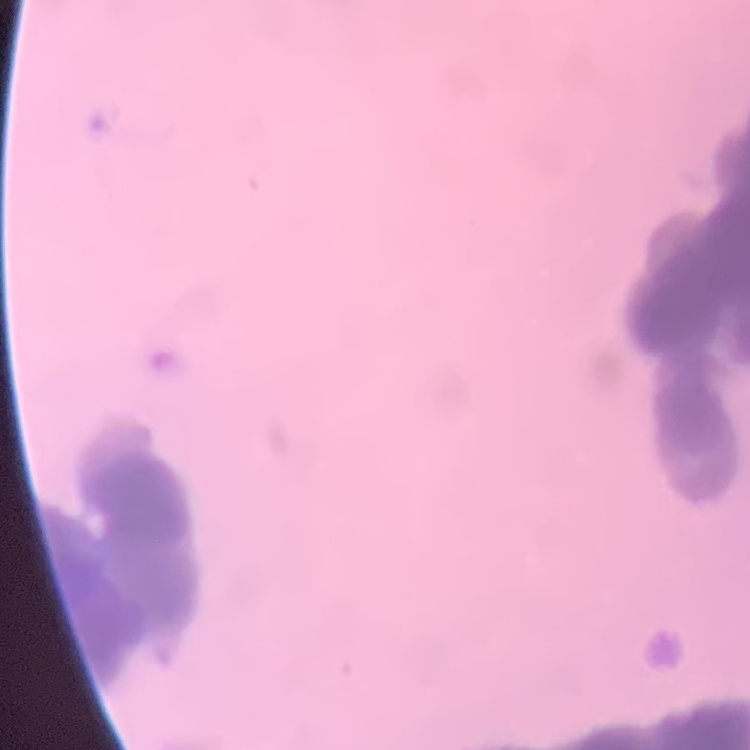

The red blood cells show rouleaux formation. Thin peripheral smear. One tile cut from a larger photomicrograph. Stained with either Field's or Giemsa.